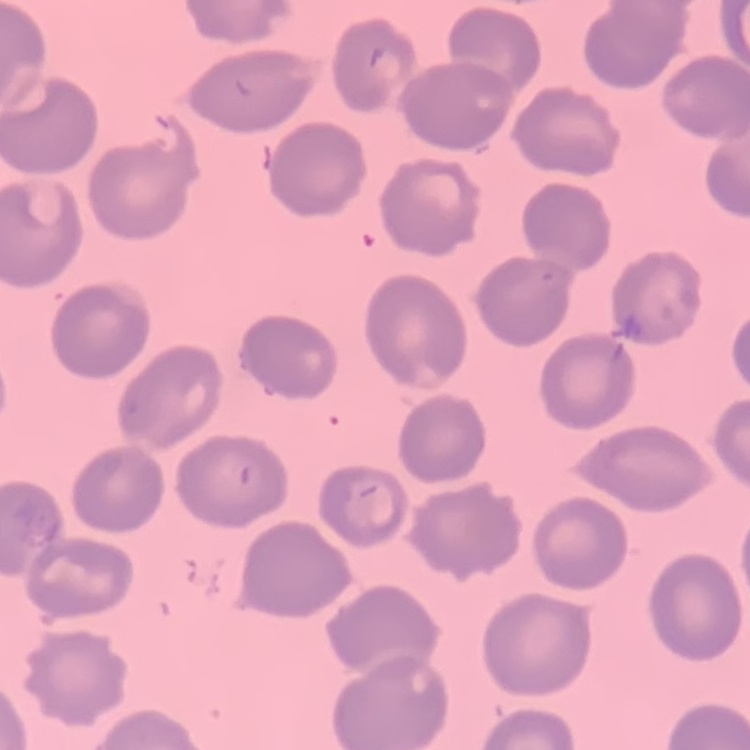 The erythrocytes show no rouleaux formation. Field's or Giemsa stain. Thin peripheral smear. One tile cut from a larger photomicrograph.